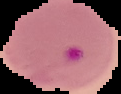
image_type: segmented cell region with the area outside set to black
image_size: 121×94 pixels
preparation: thin blood film
malaria_status: parasitized